Evaluate for Plasmodium parasites.
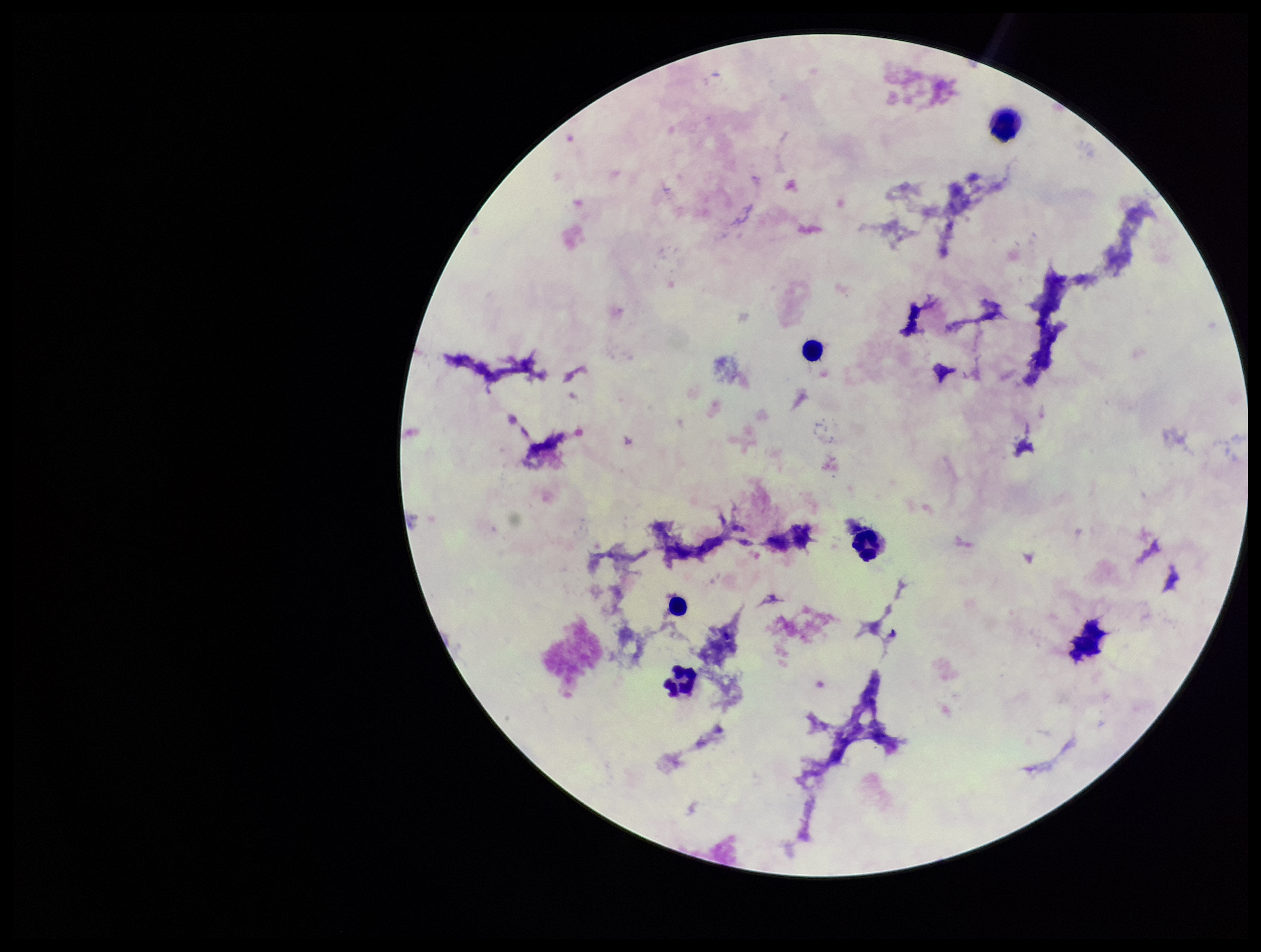

None seen.

Parasite count: 0. Image is 1261×952 pixels. Leukocyte count: 5. Patient malaria status: negative. Stained with Giemsa. Photographed through the microscope eyepiece with a smartphone camera. Preparation: thick smear. One field from this slide.